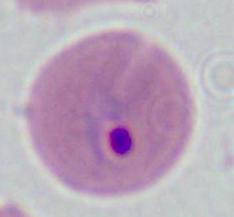
modality: micrograph
identification: Plasmodium
magnification: 400x or 1000x